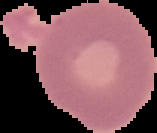
result = no Plasmodium parasites detected
image type = segmented cell region on a black background
preparation = thin blood film
image size = 157×133 pixels